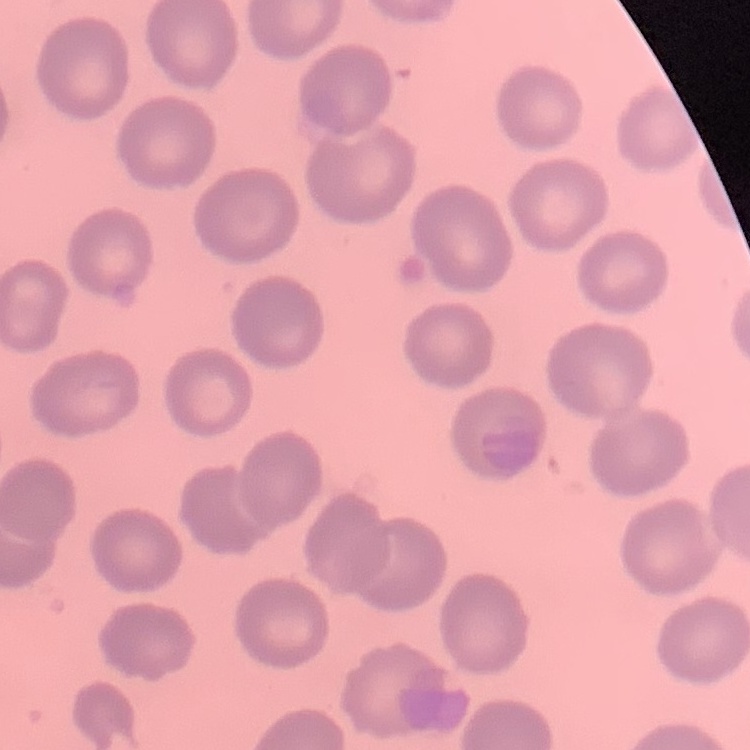

erythrocyte morphology = no rouleaux formation
image type = square crop of a larger photomicrograph
preparation = thin blood smear
stain = Field's or Giemsa